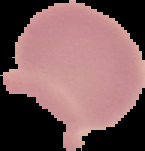
image type = segmented cell region with the area outside set to black
result = no Plasmodium parasites detected
preparation = thin blood film
image size = 145×151 pixels